Report the malaria status of this cell.
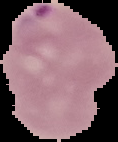
Parasitized.

Summary:
  - Image size: 118×142 pixels
  - Preparation: thin blood smear
  - Image type: cell region segmented out of the field of view; surrounding area masked to black